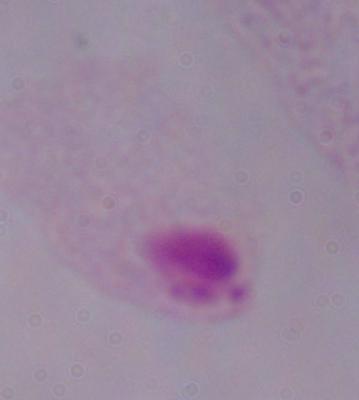 Photomicrograph. A trichomonad is seen. Captured at 1000x magnification.